Report the malaria status of this cell.
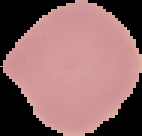

Uninfected.

{
  "image_type": "segmented cell region with the area outside set to black",
  "image_size": "142×136 pixels",
  "preparation": "thin blood film"
}